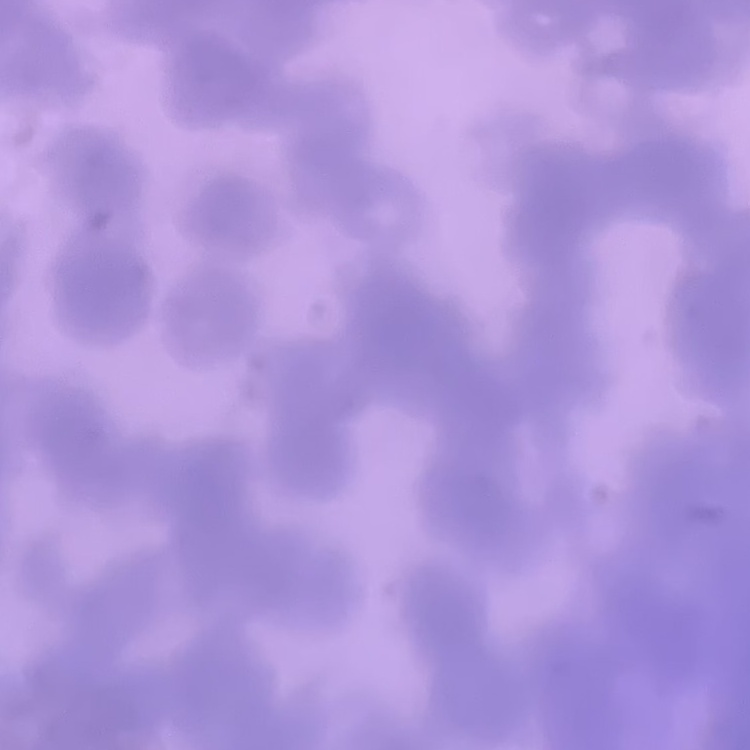 The red blood cells exhibit rouleaux formation. Thin blood smear. Stained with either Field's or Giemsa. One tile cut from a larger photomicrograph.